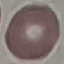

Result: negative for malaria parasites. Thin blood film. Automatically extracted cell patch, resized to 64 × 64 pixels. Giemsa stain. Photographed with a smartphone camera at the microscope eyepiece.